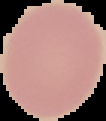
image type = segmented cell region with the area outside set to black
image size = 106×121 pixels
preparation = thin blood smear
malaria status = uninfected